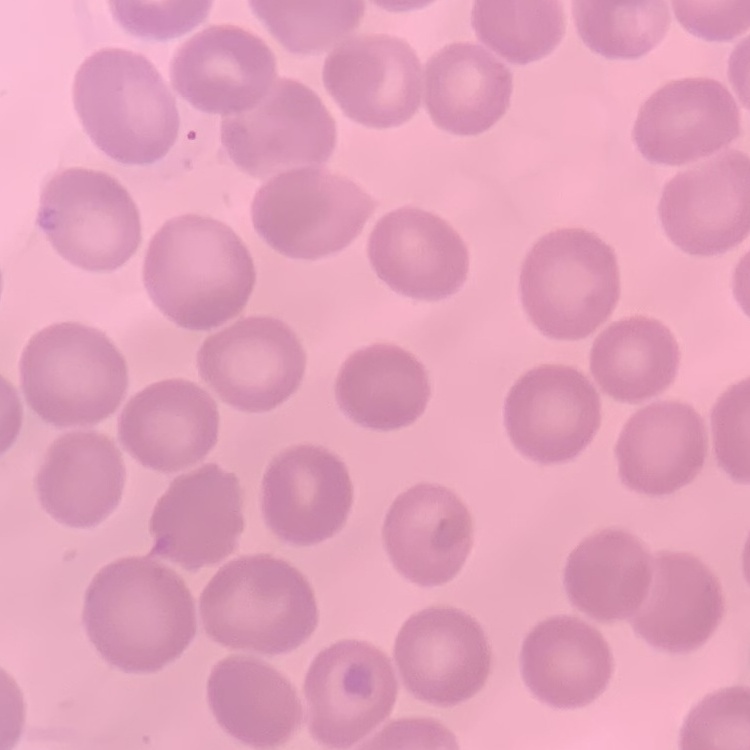
erythrocyte morphology = no rouleaux formation
stain = Field's or Giemsa
image type = one tile cut from a larger photomicrograph
preparation = thin blood film